Assess this cell for malaria.
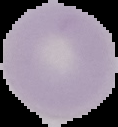
Uninfected.

image type = segmented cell region with the area outside set to black
preparation = thin blood film
image size = 118×127 pixels